Assess this cell for malaria.
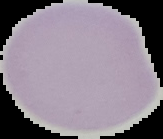

It is uninfected.

Summary:
  - Preparation: thin blood film
  - Image size: 163×139 pixels
  - Image type: cell region segmented out of the field of view; surrounding area masked to black